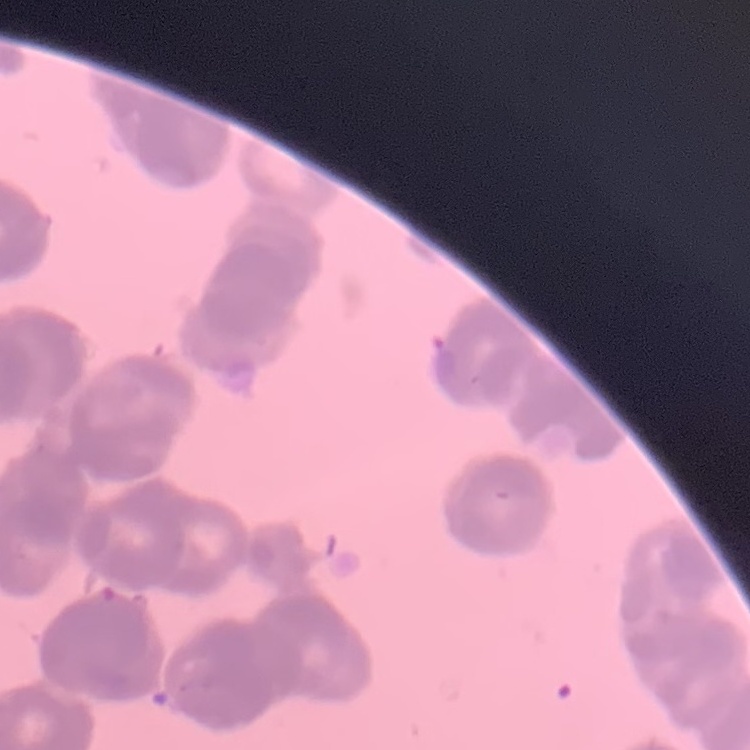
The erythrocytes exhibit rouleaux formation. Thin blood film. One tile cut from a larger photomicrograph. Field's or Giemsa stain.